Classify this cell by malaria status.
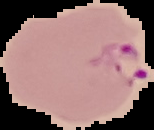
Parasitized.

Summary:
  - Image type: segmented cell region with the area outside set to black
  - Preparation: thin blood film
  - Image size: 154×130 pixels